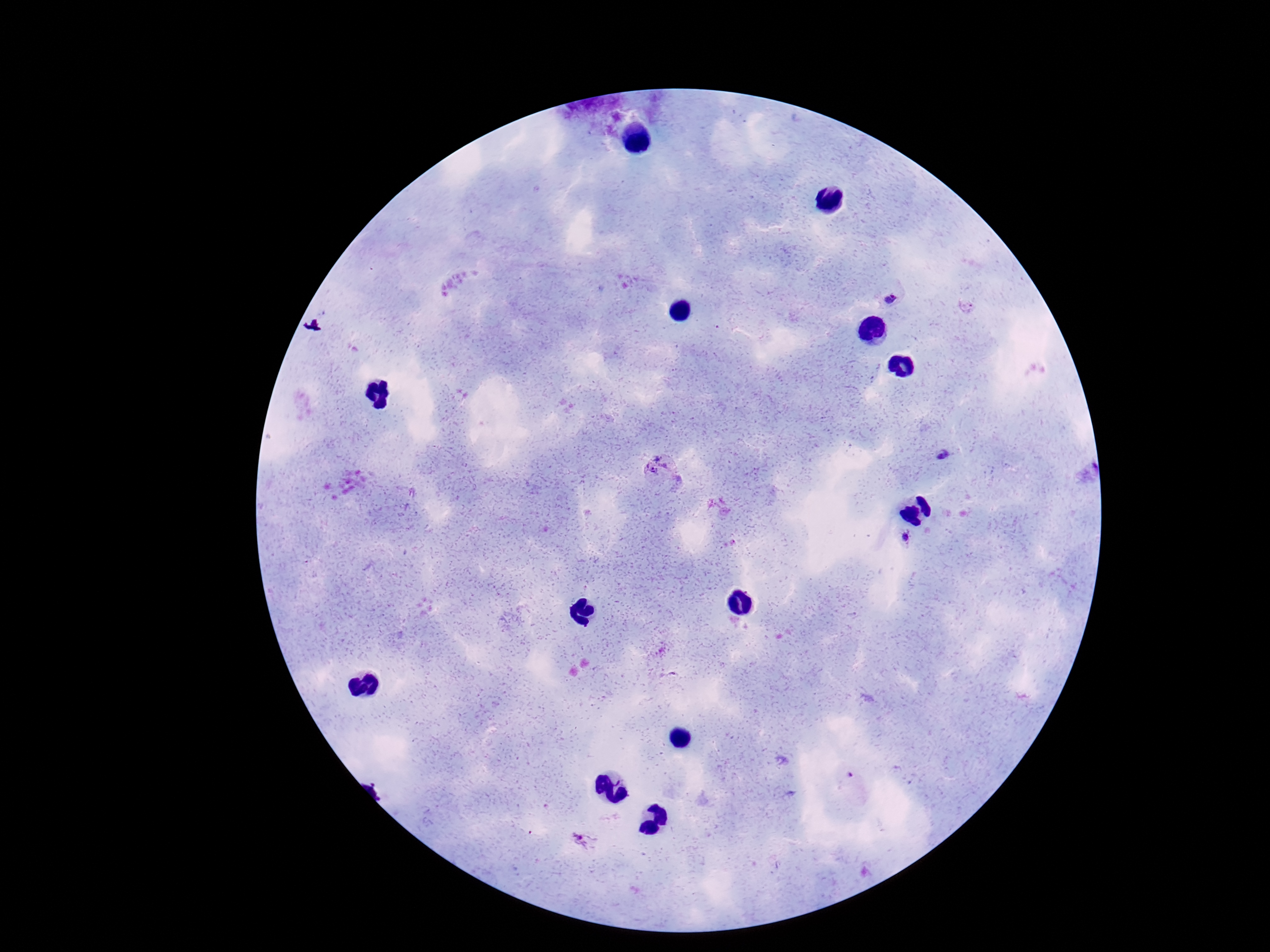
{
  "patient_malaria_status": "infected",
  "preparation": "thick blood film",
  "plasmodium_parasite_locations": "approximate centers as {x, y} in pixels: {891, 301}, {966, 306}, {944, 455}, {664, 474}, {906, 536}, {847, 777}, {587, 842}",
  "field_of_view": "single",
  "image_size": "1270×952 pixels",
  "magnification": "100x",
  "stain": "Giemsa",
  "capture": "smartphone camera through the microscope eyepiece"
}